Comment on the morphology of the red blood cells.
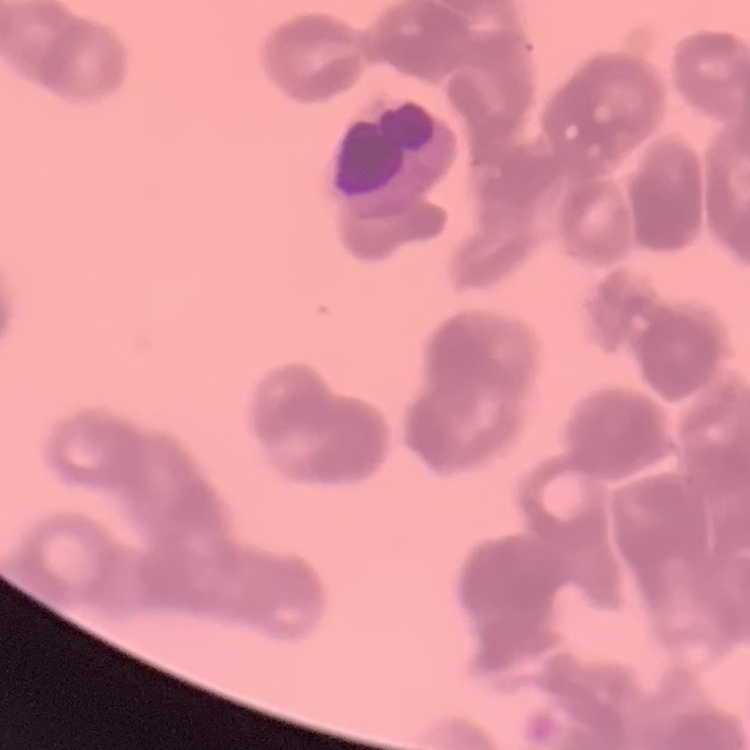
Rouleaux formation.

Summary:
  - Image type: one tile cut from a larger photomicrograph
  - Preparation: thin blood smear
  - Stain: Field's or Giemsa